Point out each malaria parasite and classify it by life-cycle stage.
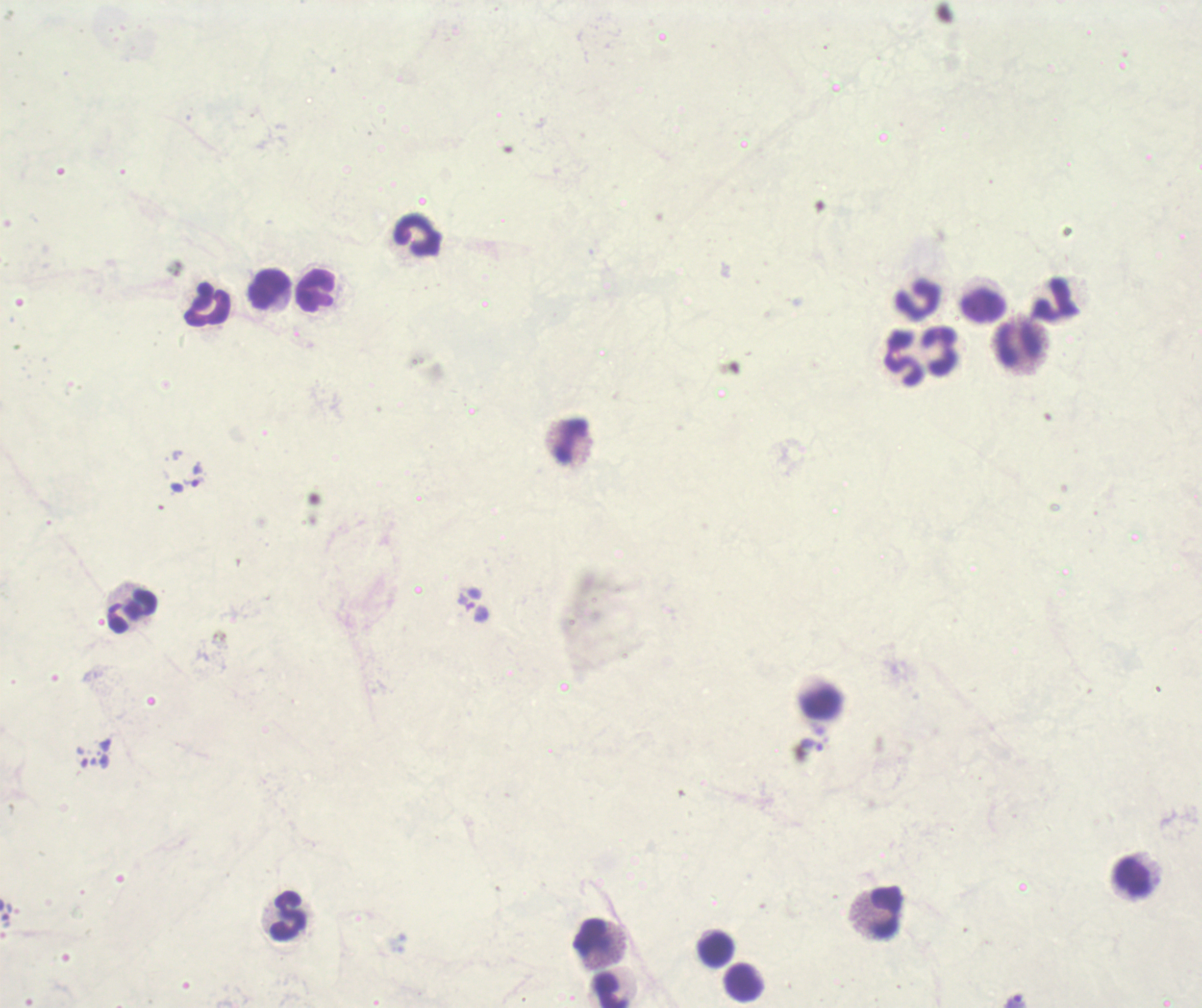

Approximate object centers, in pixels from the top-left corner.
Trophozoites: (x=194, y=481), (x=813, y=743), (x=1015, y=999).
No schizont or gametocyte forms observed.

Approximate object centers, in pixels from the top-left corner.
Summary:
  - Leukocyte locations: (x=419, y=237), (x=270, y=290), (x=315, y=291), (x=918, y=299), (x=1056, y=299), (x=211, y=305), (x=985, y=307), (x=1019, y=345), (x=939, y=352), (x=904, y=357), (x=571, y=440), (x=134, y=612), (x=820, y=704), (x=1134, y=878), (x=885, y=911), (x=286, y=916), (x=592, y=938), (x=717, y=950), (x=744, y=982), (x=611, y=989)
  - Magnification: 100x
  - Image size: 1202×1008 pixels
  - Context: previously used in an actual diagnosis
  - Coloration quality: bad
  - Background quality: poor
  - Stain: Romanowsky
  - Field of view: single
  - Preparation: thick smear of blood